Locate every Plasmodium malariae-infected red blood cell.
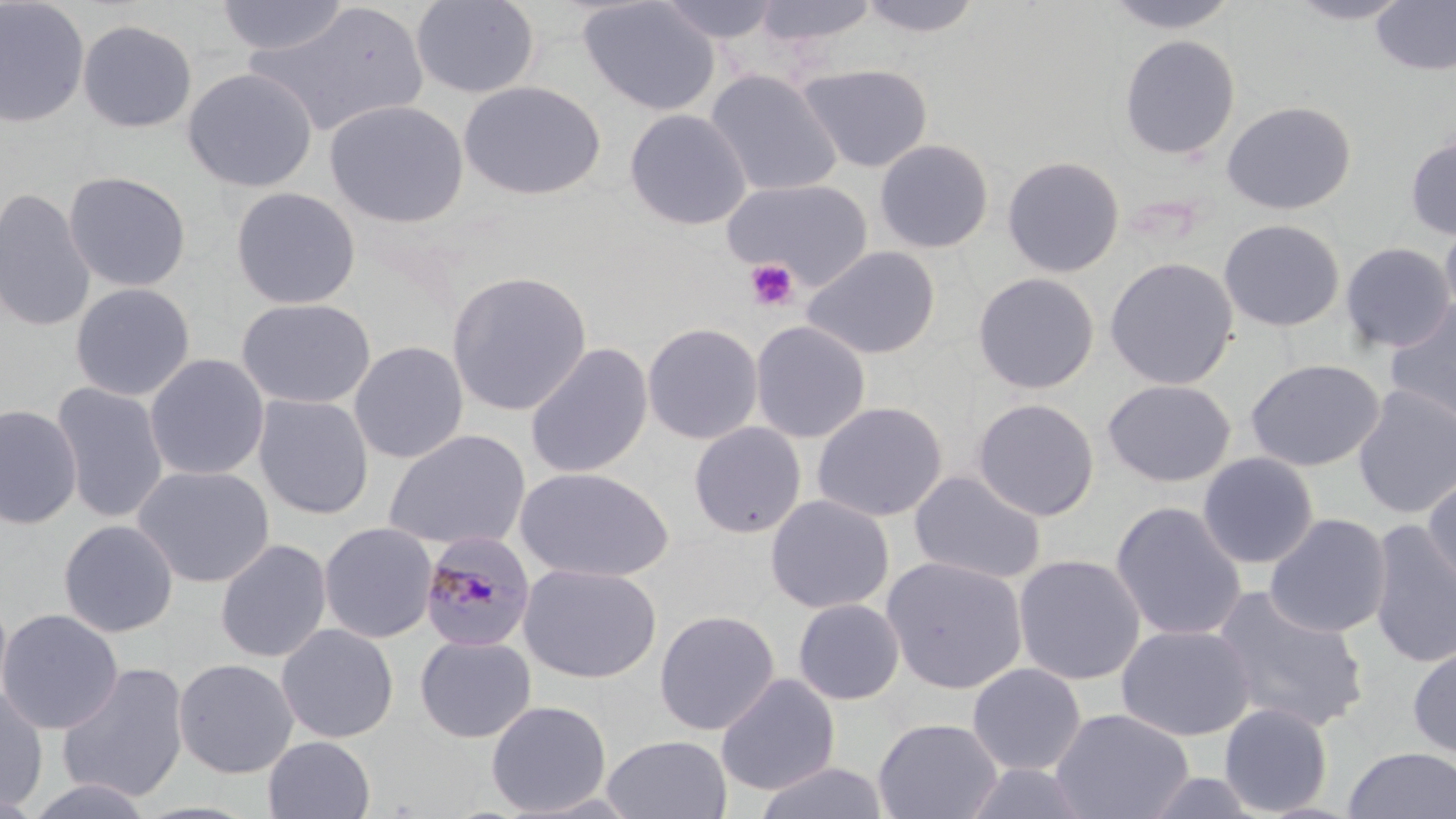

Approximate bounding boxes as [x1, y1, x2, y2] in pixels.
Plasmodium malariae-infected red blood cells: [420, 530, 539, 653].

Summary:
  - Platelet locations: [744, 258, 801, 312]
  - Uninfected red blood cell locations: [0, 0, 90, 128], [215, 0, 351, 57], [410, 0, 541, 99], [578, 0, 720, 116], [655, 0, 781, 44], [751, 0, 879, 48], [856, 0, 986, 39], [1100, 0, 1243, 34], [1284, 0, 1416, 24], [1371, 1, 1456, 76], [247, 3, 430, 137], [77, 19, 197, 133], [1119, 34, 1240, 159], [797, 63, 933, 172], [182, 67, 318, 193], [706, 69, 843, 197], [459, 81, 606, 201], [324, 99, 469, 228], [1221, 100, 1356, 215], [623, 109, 752, 231], [1404, 135, 1456, 241], [874, 138, 994, 253], [1001, 155, 1125, 278], [63, 171, 191, 292], [722, 177, 873, 288], [230, 186, 361, 309], [0, 188, 97, 333], [1440, 217, 1456, 325], [1218, 218, 1345, 332], [1339, 242, 1455, 353], [801, 246, 941, 360], [1104, 256, 1239, 390], [446, 270, 593, 416], [972, 272, 1100, 394], [70, 283, 195, 401], [1383, 297, 1456, 429], [236, 298, 376, 410], [750, 320, 872, 444], [642, 322, 764, 445], [349, 340, 469, 464], [524, 341, 654, 479], [144, 354, 270, 482], [1244, 358, 1384, 471], [1102, 379, 1235, 487], [51, 381, 169, 524], [1352, 384, 1456, 521], [253, 394, 374, 520], [972, 398, 1100, 521], [811, 400, 948, 522], [0, 404, 82, 530], [688, 421, 807, 538], [383, 428, 531, 552], [1197, 452, 1319, 569], [133, 465, 275, 588], [515, 466, 675, 583], [1422, 467, 1456, 593], [908, 470, 1047, 585], [765, 494, 894, 614], [1110, 501, 1247, 642], [1264, 513, 1392, 638], [58, 519, 179, 638], [1367, 519, 1456, 671], [318, 522, 438, 643], [214, 538, 332, 663], [1012, 553, 1146, 686], [881, 556, 1028, 694], [518, 562, 662, 684], [1210, 585, 1369, 734], [793, 598, 905, 705], [0, 609, 124, 734], [654, 609, 780, 736], [277, 623, 399, 743], [1116, 624, 1255, 741], [415, 634, 537, 743], [1407, 643, 1456, 760], [173, 658, 298, 778], [55, 662, 190, 804], [967, 662, 1086, 776], [716, 673, 840, 796], [0, 686, 49, 812], [486, 699, 611, 816], [1219, 703, 1333, 816], [1050, 707, 1194, 819], [873, 717, 1003, 819], [601, 734, 732, 819], [263, 735, 375, 819], [1342, 745, 1456, 819], [753, 760, 889, 819], [962, 762, 1095, 819], [1141, 771, 1263, 818], [21, 777, 157, 819], [0, 789, 46, 819]
  - Slide-level diagnosis: Plasmodium malariae
  - Image size: 1456×819 pixels
  - Field of view: single
  - Magnification: 1000x
  - Stain: May-Grünwald-Giemsa
  - Preparation: thin blood film
  - Modality: optical microscopy